Outline platelets.
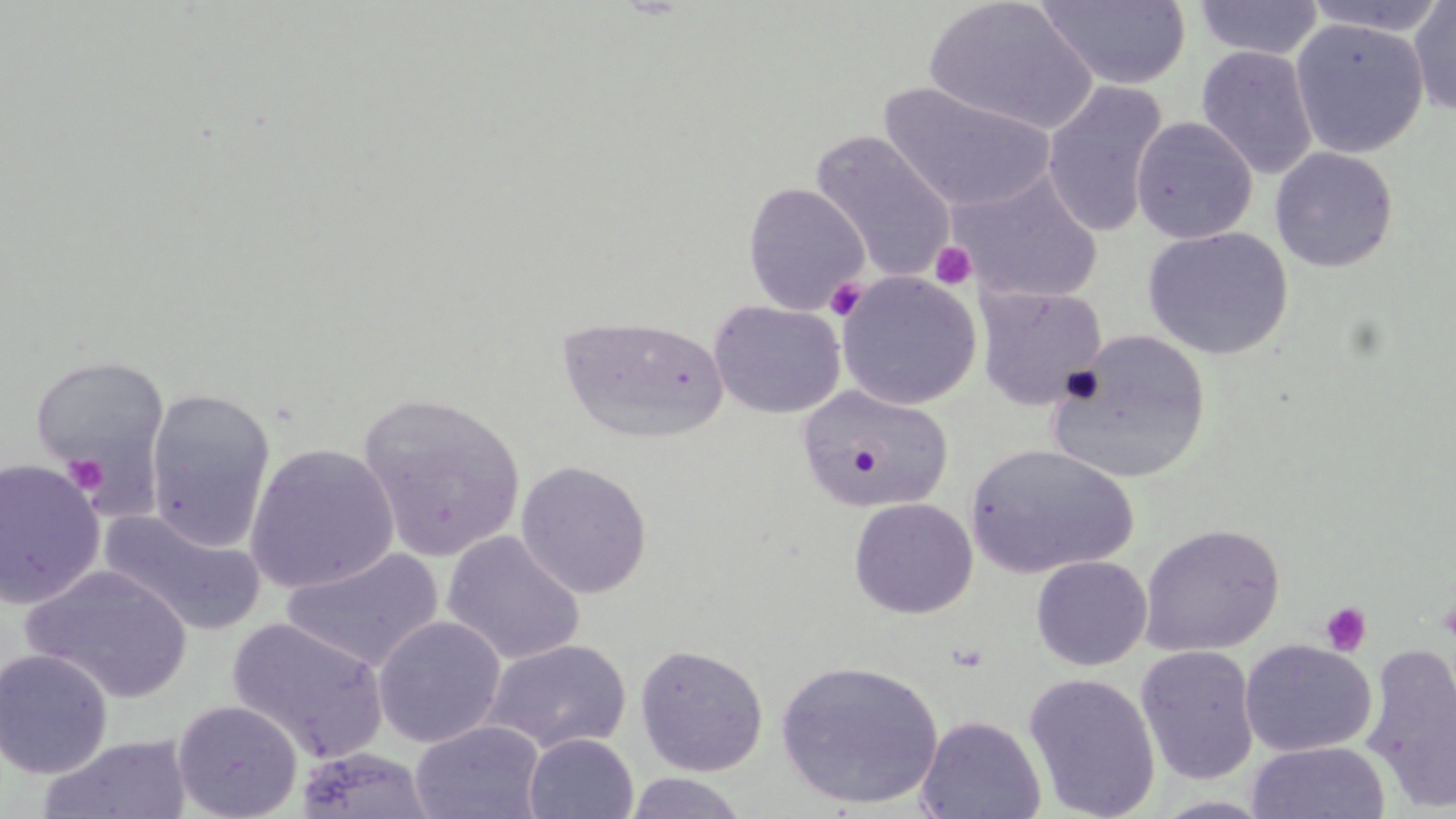
Approximate bounding boxes as (x1,y1)-(x2,y2) corner pairs in pixels.
Platelets: (930,241)-(977,290), (825,277)-(867,321), (63,454)-(108,496), (1320,602)-(1372,656).

Uninfected red blood cell locations: (924,0)-(1098,136), (1036,0)-(1192,90), (1304,0)-(1450,37), (1407,0)-(1456,116), (1195,1)-(1324,60), (1290,18)-(1429,159), (1195,45)-(1319,180), (1041,80)-(1168,239), (880,81)-(1057,214), (1131,117)-(1258,245), (810,131)-(957,284), (1269,147)-(1398,273), (951,172)-(1102,306), (742,182)-(870,315), (1142,227)-(1293,360), (836,271)-(983,411), (975,286)-(1107,410), (709,300)-(846,419), (558,314)-(730,444), (1047,329)-(1212,484), (29,354)-(171,490), (796,384)-(955,512), (143,386)-(276,551), (358,391)-(526,563), (244,443)-(399,594), (965,443)-(1138,579), (0,458)-(105,609), (515,460)-(653,599), (848,497)-(977,618), (100,509)-(266,637), (1139,524)-(1285,657), (441,530)-(586,666), (281,548)-(443,672), (1030,555)-(1152,671), (22,565)-(192,703), (372,615)-(506,748), (227,617)-(389,764), (482,638)-(632,754), (1240,639)-(1377,757), (1360,642)-(1456,814), (634,643)-(769,777), (1135,646)-(1260,785), (0,649)-(113,779), (775,659)-(944,810), (1023,672)-(1161,819), (171,699)-(304,819), (915,714)-(1047,819), (409,720)-(546,819), (523,732)-(638,818), (37,734)-(194,819), (1246,741)-(1390,819), (294,747)-(436,819), (623,772)-(749,818), (1149,795)-(1278,818). Slide-level diagnosis: no evidence of blood parasites. Light microscopy. Single field of view. Thin blood smear. Image is 1456×819 pixels. 1000x magnification. May-Grünwald-Giemsa stain.